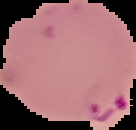

{
  "image_size": "136×130 pixels",
  "image_type": "segmented cell region on a black background",
  "result": "malaria parasites detected",
  "preparation": "thin blood smear"
}